Locate every blood parasite and identify its species.
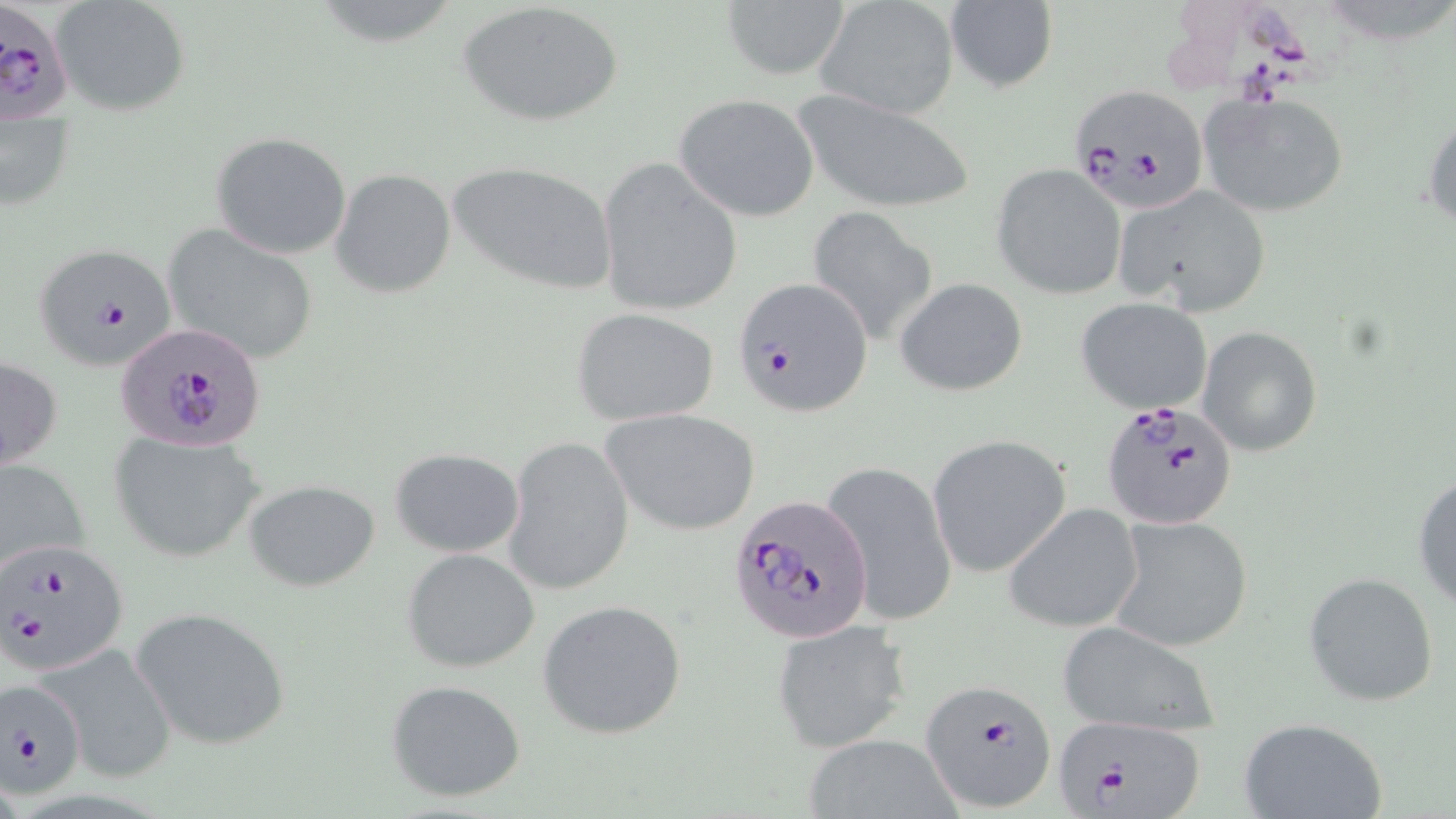

Approximate bounding boxes as (x1, y1, x2, y2) in pixels.
Plasmodium falciparum-infected red blood cells: (0, 0, 74, 123), (1070, 84, 1209, 212), (32, 242, 176, 371), (734, 276, 871, 416), (117, 322, 265, 453), (1100, 399, 1239, 532), (730, 492, 875, 643), (1, 536, 130, 675), (922, 678, 1058, 812), (1, 679, 86, 800), (1051, 710, 1207, 818).
No Plasmodium ovale, Plasmodium malariae, Plasmodium vivax, Babesia divergens, or Trypanosoma brucei observed.

slide-level diagnosis = Plasmodium falciparum
field of view = one of a larger specimen
stain = May-Grünwald-Giemsa
uninfected red blood cell locations = approximate bounding boxes as (x1, y1, x2, y2) in pixels: (52, 0, 191, 117), (943, 1, 1057, 93), (459, 2, 625, 128), (719, 2, 848, 80), (815, 2, 960, 121), (1196, 88, 1351, 218), (790, 89, 976, 215), (675, 93, 820, 222), (1424, 104, 1456, 235), (210, 130, 352, 259), (595, 159, 743, 318), (447, 161, 618, 294), (992, 164, 1126, 298), (330, 169, 456, 298), (1113, 183, 1272, 315), (806, 206, 940, 344), (162, 223, 321, 367), (895, 277, 1028, 396), (1076, 297, 1213, 415), (572, 307, 719, 425), (1198, 325, 1324, 457), (1, 355, 63, 473), (601, 407, 762, 536), (109, 430, 266, 563), (929, 433, 1070, 575), (503, 435, 634, 597), (390, 448, 525, 558), (0, 456, 91, 579), (827, 460, 956, 633), (1412, 471, 1456, 610), (243, 479, 379, 591), (1003, 503, 1143, 633), (1105, 515, 1255, 655), (401, 548, 540, 673), (1303, 572, 1439, 707), (537, 599, 686, 740), (129, 605, 292, 751), (769, 617, 911, 752), (1055, 621, 1221, 738), (43, 641, 173, 779), (385, 678, 527, 803), (1237, 717, 1390, 819), (798, 734, 965, 819)
modality = optical microscopy
preparation = thin blood smear
image size = 1456×819 pixels
magnification = 1000x